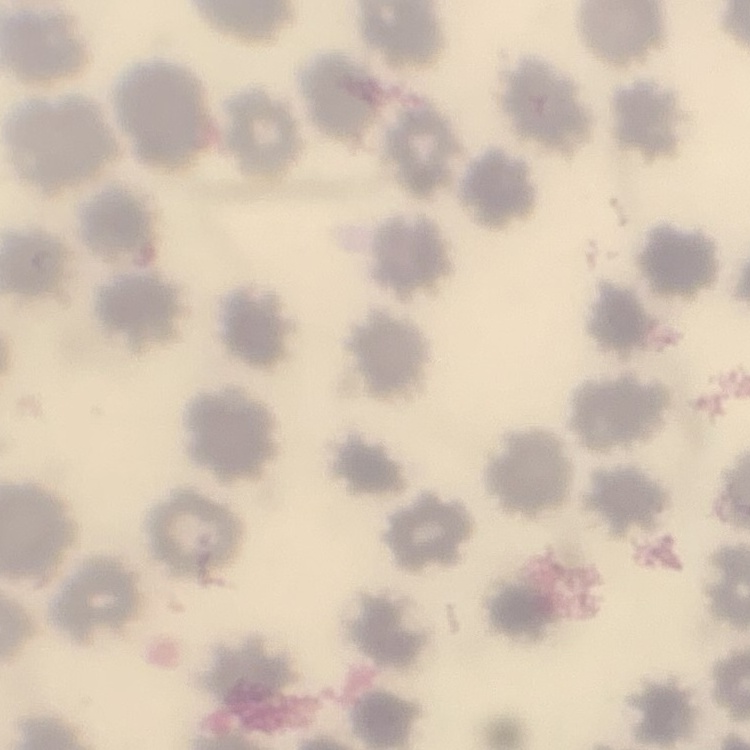

The red blood cells exhibit no rouleaux formation. Field's or Giemsa stain. Thin blood smear. Square crop of a larger photomicrograph.